Give the preparation type.
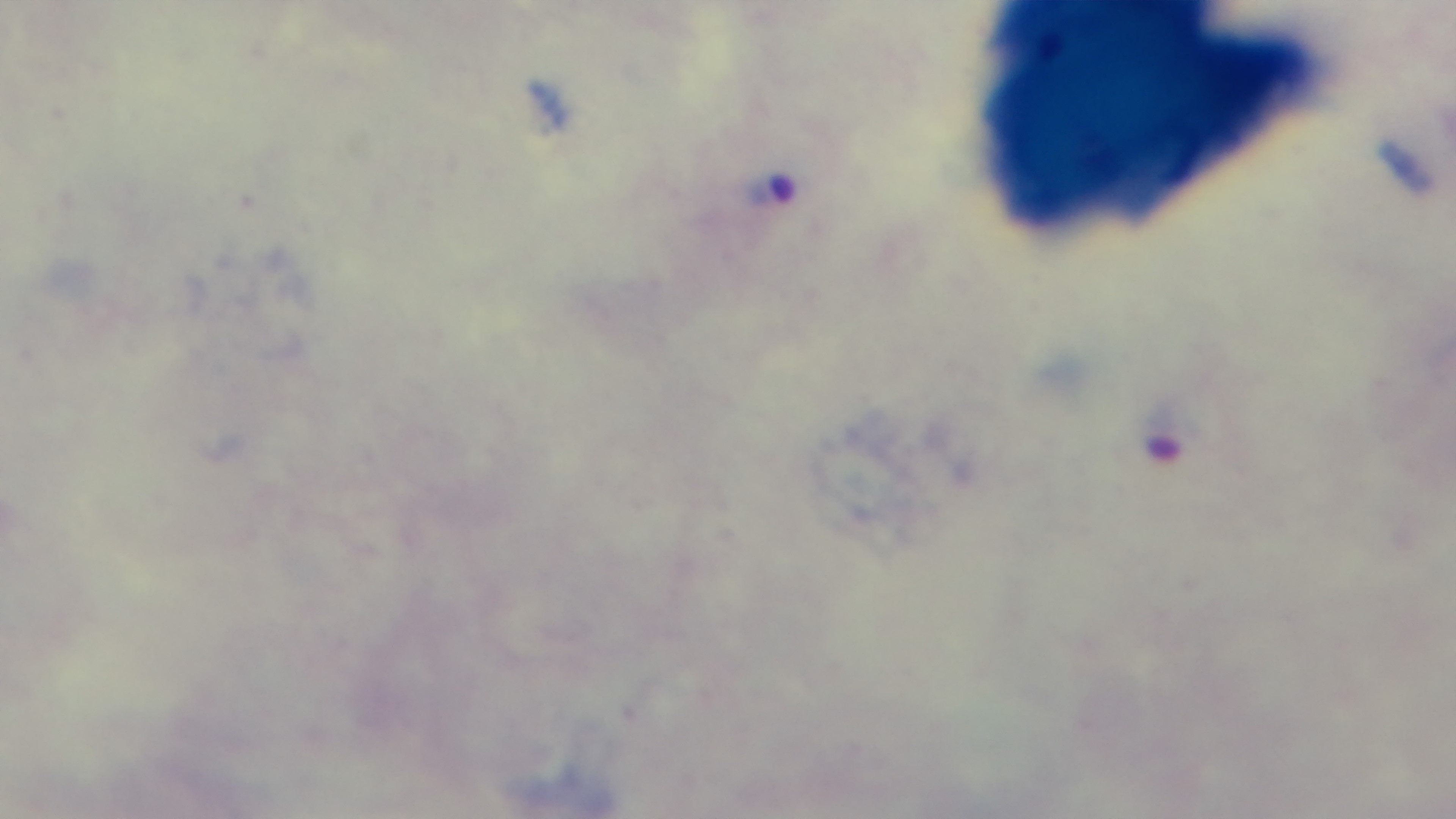
It is a thick blood film.

Captured with a mounted 4K digital camera. Giemsa stain. 100x oil-immersion objective. Malaria status: infected. Photomicrograph. Single field of view.